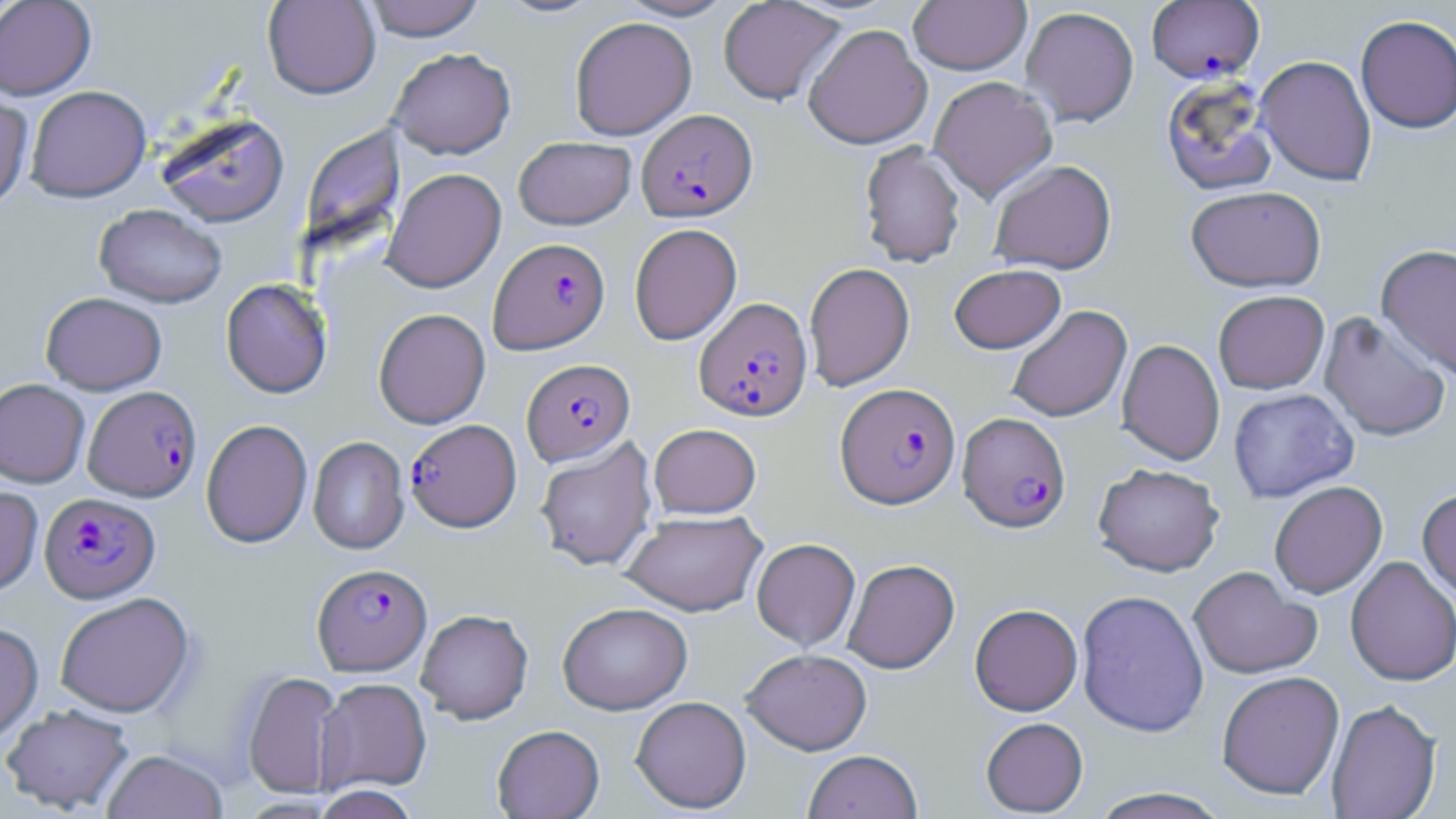
Approximate bounding boxes as [x1, y1, x2, y2] in pixels. Uninfected red blood cell locations: [0, 0, 96, 100], [263, 0, 380, 99], [362, 0, 486, 41], [494, 0, 607, 19], [616, 0, 737, 21], [908, 0, 1031, 75], [718, 1, 846, 106], [1020, 6, 1140, 128], [1355, 15, 1456, 134], [569, 16, 697, 140], [803, 23, 932, 150], [389, 47, 516, 159], [1256, 55, 1377, 186], [1160, 75, 1279, 196], [928, 76, 1058, 202], [25, 85, 151, 202], [0, 90, 33, 214], [157, 114, 290, 228], [307, 117, 403, 262], [513, 136, 636, 230], [859, 141, 966, 268], [988, 159, 1117, 274], [382, 168, 506, 293], [1185, 185, 1326, 292], [94, 204, 227, 308], [629, 223, 742, 345], [1376, 244, 1456, 381], [804, 262, 915, 391], [949, 264, 1065, 353], [221, 279, 333, 398], [1213, 290, 1329, 394], [40, 292, 167, 395], [1007, 305, 1132, 422], [374, 308, 490, 429], [1319, 310, 1451, 443], [1117, 339, 1225, 465], [0, 379, 90, 488], [1227, 388, 1359, 503], [201, 419, 312, 548], [649, 423, 761, 518], [308, 436, 410, 554], [534, 437, 657, 571], [1093, 463, 1224, 576], [1269, 481, 1387, 598], [0, 485, 43, 598], [1417, 487, 1456, 600], [621, 510, 767, 617], [751, 538, 861, 651], [1345, 556, 1456, 686], [843, 558, 959, 674], [1188, 566, 1321, 680], [1076, 589, 1209, 738], [54, 592, 195, 718], [557, 602, 692, 715], [969, 603, 1083, 716], [416, 609, 534, 724], [0, 623, 43, 746], [741, 648, 872, 755], [241, 670, 342, 799], [1216, 671, 1345, 800], [315, 677, 432, 795], [631, 696, 751, 813], [1326, 699, 1442, 819], [1, 704, 135, 814], [980, 717, 1088, 816], [492, 724, 605, 818], [101, 750, 228, 819], [803, 750, 922, 819], [311, 786, 420, 819], [1087, 787, 1233, 819]. Plasmodium falciparum-infected red blood cell locations: [1146, 1, 1265, 83], [637, 109, 757, 221], [489, 237, 610, 354], [694, 296, 812, 421], [522, 358, 635, 466], [835, 382, 960, 508], [83, 385, 201, 501], [958, 411, 1071, 532], [405, 419, 521, 532], [39, 492, 161, 603], [313, 563, 432, 675]. Slide-level diagnosis: Plasmodium falciparum. Image is 1456×819 pixels. Single field of view. Optical microscopy. May-Grünwald-Giemsa-stained preparation. Thin blood smear. Captured at 1000x magnification.